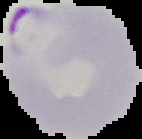
image_size: 142×139 pixels
result: Plasmodium parasites detected
image_type: segmented cell region with the area outside set to black
preparation: thin blood film